Assess the morphology of the red blood cells.
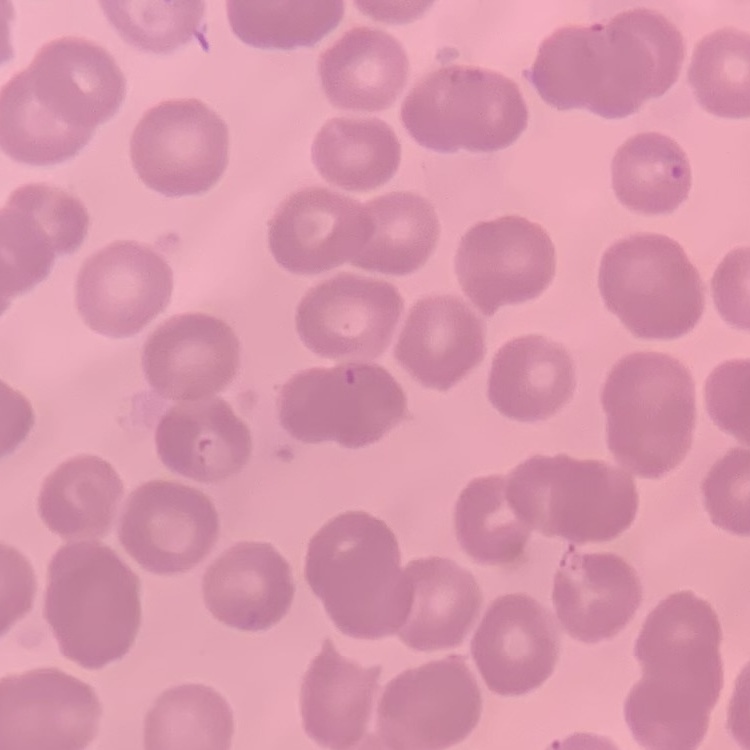
They show no rouleaux formation.

Summary:
  - Stain: Field's or Giemsa
  - Preparation: thin blood smear
  - Image type: square crop of a larger photomicrograph